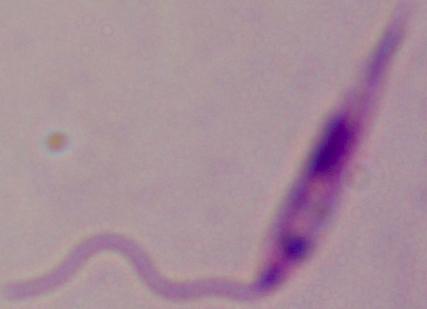
modality = micrograph
identification = Leishmania
magnification = 1000x